Give the extent of all Plasmodium parasites.
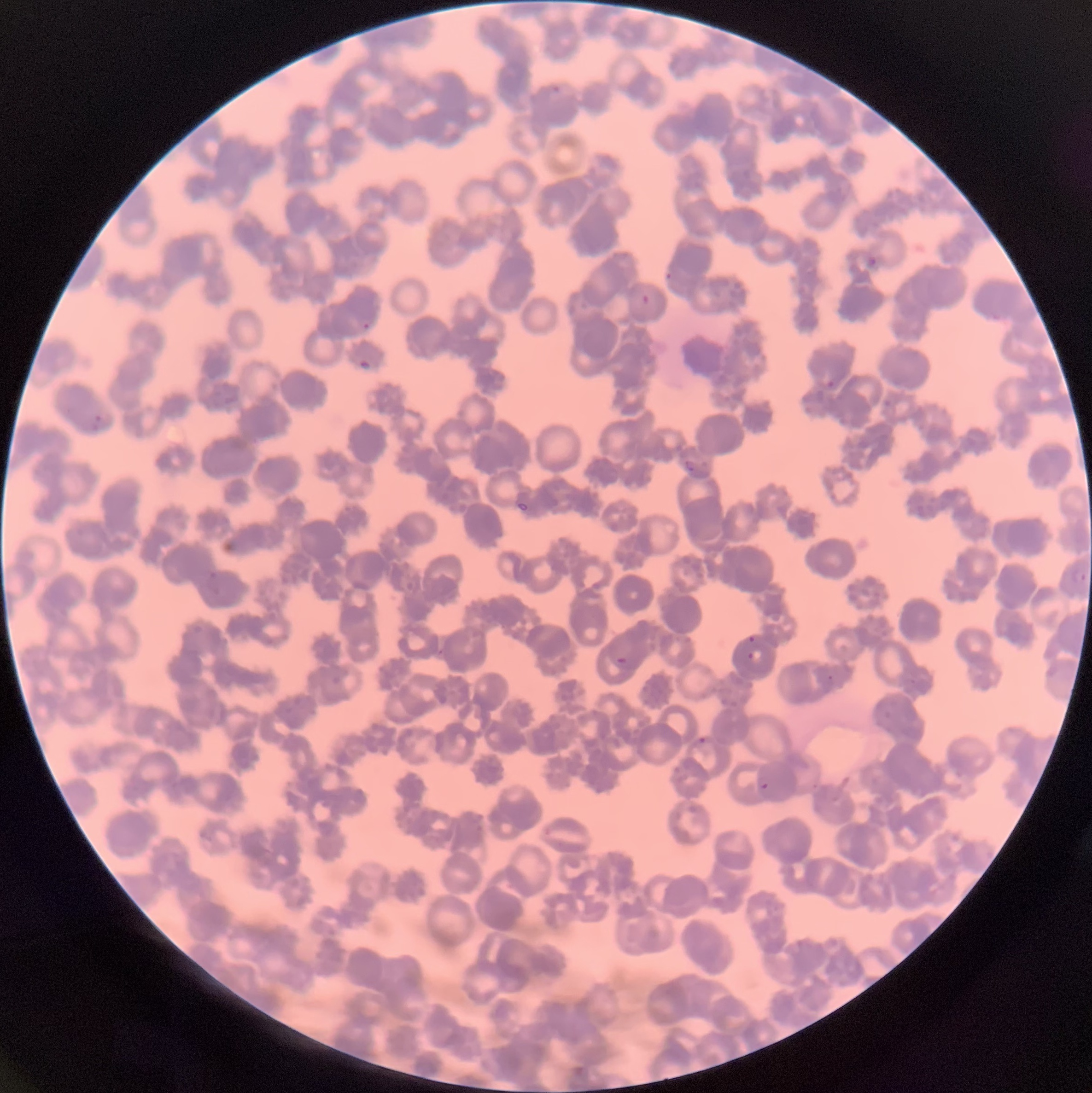
Approximate bounding boxes as named x1/y1/x2/y2 corners in pixels.
Plasmodium parasites: (x1=549, y1=84, x2=562, y2=95), (x1=865, y1=256, x2=878, y2=268), (x1=666, y1=272, x2=672, y2=282), (x1=642, y1=295, x2=649, y2=305), (x1=361, y1=322, x2=370, y2=330), (x1=358, y1=358, x2=370, y2=372), (x1=826, y1=381, x2=834, y2=387), (x1=91, y1=413, x2=102, y2=430), (x1=684, y1=460, x2=695, y2=472), (x1=517, y1=502, x2=528, y2=512), (x1=1073, y1=569, x2=1086, y2=584), (x1=204, y1=571, x2=222, y2=595), (x1=747, y1=635, x2=756, y2=642), (x1=748, y1=650, x2=762, y2=663), (x1=615, y1=655, x2=635, y2=667), (x1=822, y1=675, x2=834, y2=690), (x1=696, y1=737, x2=708, y2=743), (x1=754, y1=774, x2=769, y2=790).

Summary:
  - Image size: 1092×1093 pixels
  - Modality: light microscopy
  - Red blood cell morphology: rouleaux formation
  - Preparation: thin blood film